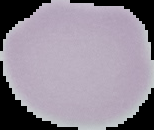

Summary:
  - Image type: segmented cell region on a black background
  - Preparation: thin blood smear
  - Image size: 154×130 pixels
  - Malaria status: uninfected